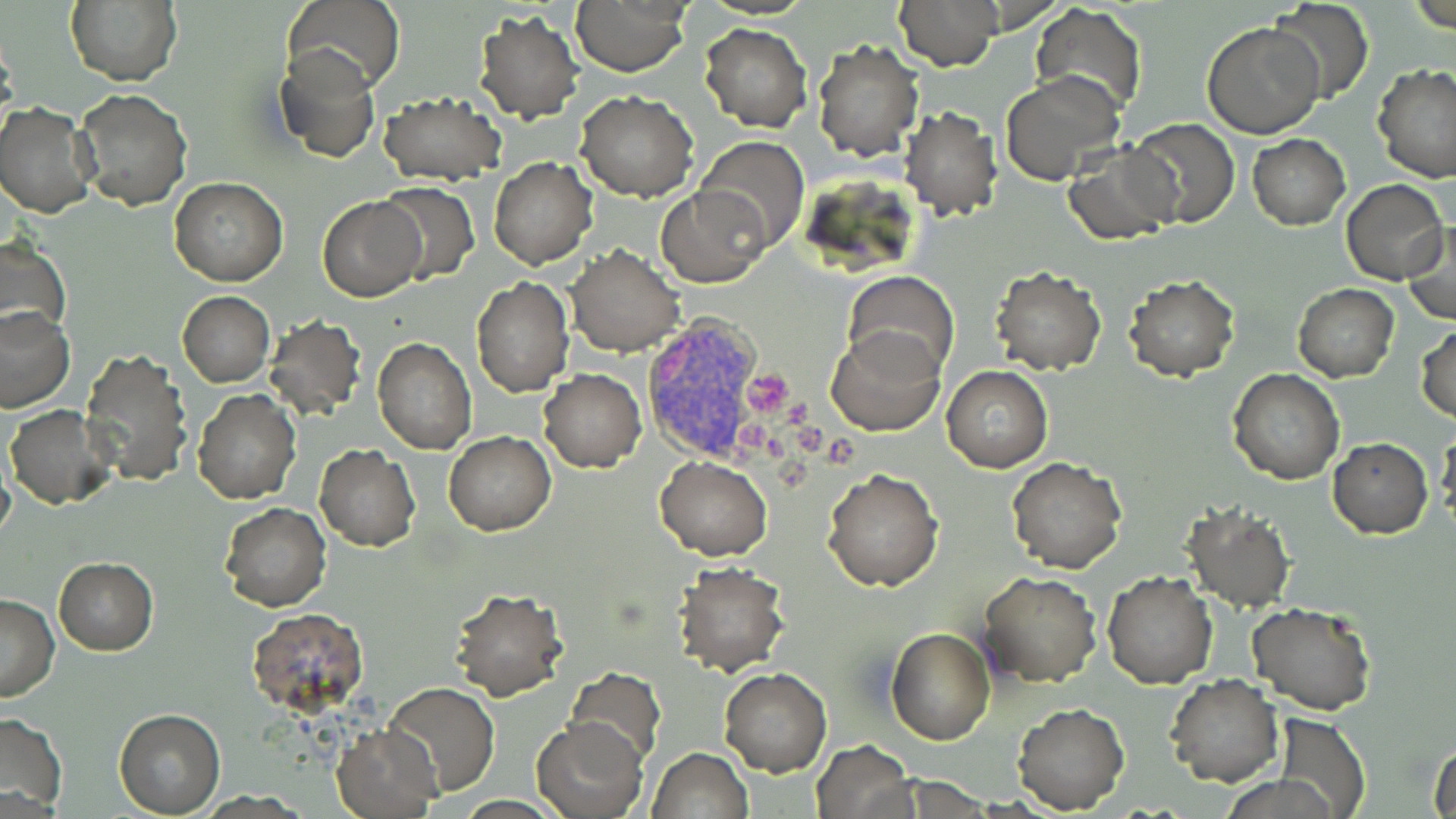

Approximate bounding boxes as [x1, y1, x2, y2] in pixels. Uninfected red blood cell locations: [284, 0, 406, 93], [896, 0, 1001, 70], [1270, 0, 1374, 103], [65, 2, 182, 86], [571, 2, 690, 76], [1030, 4, 1148, 114], [473, 12, 585, 124], [1203, 20, 1325, 138], [699, 22, 812, 132], [812, 38, 923, 160], [274, 45, 380, 163], [1372, 63, 1456, 182], [1000, 70, 1126, 184], [75, 88, 193, 211], [377, 88, 506, 186], [576, 91, 699, 202], [1, 103, 95, 218], [898, 106, 1003, 221], [1128, 118, 1239, 228], [1247, 134, 1349, 230], [696, 137, 809, 252], [1062, 145, 1180, 245], [490, 157, 598, 269], [170, 178, 288, 286], [1341, 179, 1448, 285], [375, 184, 480, 284], [658, 185, 769, 288], [318, 198, 425, 301], [1402, 219, 1455, 325], [0, 236, 71, 343], [566, 244, 685, 356], [991, 267, 1107, 374], [843, 270, 959, 378], [1123, 275, 1239, 382], [471, 278, 572, 397], [1293, 284, 1399, 382], [177, 291, 275, 387], [0, 306, 74, 413], [263, 314, 368, 421], [824, 324, 944, 436], [1415, 324, 1456, 421], [372, 338, 477, 455], [81, 349, 192, 486], [943, 365, 1052, 472], [1227, 367, 1344, 483], [539, 368, 646, 473], [193, 389, 302, 504], [7, 405, 118, 510], [1436, 425, 1456, 524], [445, 431, 556, 535], [1327, 438, 1433, 537], [315, 444, 420, 550], [1005, 455, 1126, 573], [655, 456, 774, 560], [823, 467, 943, 592], [220, 502, 331, 612], [1181, 505, 1295, 612], [53, 557, 157, 655], [673, 563, 789, 676], [979, 571, 1102, 686], [1101, 572, 1217, 690], [448, 586, 568, 700], [0, 594, 59, 701], [1247, 602, 1378, 715], [245, 609, 369, 710], [885, 627, 996, 744], [565, 667, 667, 767], [720, 668, 830, 775], [1165, 674, 1283, 787], [384, 682, 499, 796], [1013, 702, 1129, 814], [114, 710, 225, 817], [0, 711, 68, 813], [1274, 712, 1372, 819], [534, 720, 645, 815], [332, 723, 442, 818], [1429, 735, 1456, 819], [811, 739, 914, 819], [647, 747, 753, 819]. Plasmodium vivax-infected red blood cell locations: [640, 315, 774, 461]. Platelet locations: [744, 370, 791, 419], [779, 396, 813, 429], [735, 420, 772, 453], [796, 420, 826, 454], [824, 432, 857, 465], [776, 455, 812, 492]. Slide-level diagnosis: Plasmodium vivax. Single field of view. Optical microscopy. May-Grünwald-Giemsa stain. Image is 1456×819 pixels. 1000x magnification. Thin blood smear.